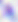
Photomicrograph. 400x magnification. Toxoplasma gondii is seen.